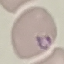

Summary:
  - Malaria status: parasitized
  - Preparation: thin smear
  - Stain: Giemsa
  - Image type: automatically extracted cell patch, resized to 64 × 64 pixels
  - Capture: smartphone through the microscope eyepiece